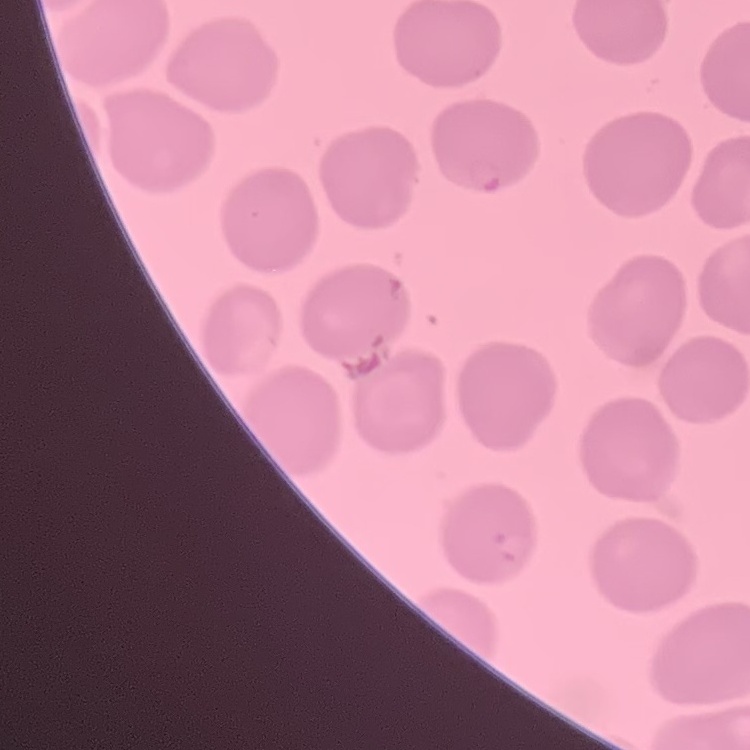

The red blood cells exhibit no rouleaux formation. Square crop of a larger photomicrograph. Thin blood film. Field's or Giemsa stain.